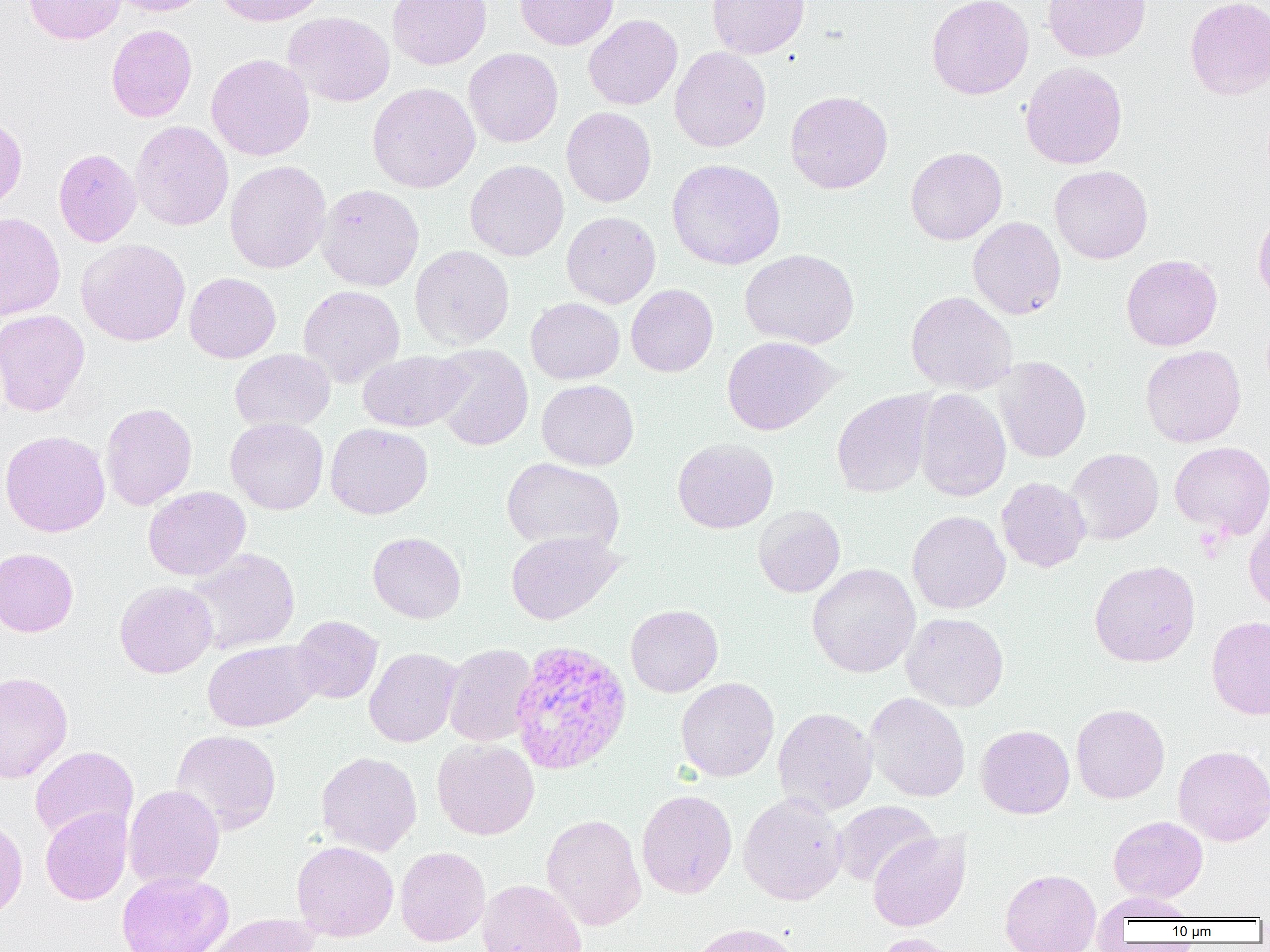
Approximate bounding boxes as (x1, y1, x2, y2) in pixels. Uninfected red blood cell locations: (24, 0, 125, 44), (110, 0, 210, 16), (214, 0, 331, 27), (387, 0, 491, 69), (515, 0, 619, 50), (706, 0, 809, 59), (926, 0, 1034, 99), (1042, 0, 1151, 62), (1184, 0, 1270, 100), (282, 11, 396, 107), (583, 14, 682, 109), (106, 24, 197, 122), (669, 46, 772, 152), (464, 48, 563, 148), (206, 53, 315, 161), (1020, 61, 1128, 169), (367, 82, 480, 193), (785, 90, 893, 194), (561, 107, 656, 207), (0, 111, 27, 212), (130, 120, 234, 231), (905, 147, 1007, 245), (53, 148, 142, 247), (465, 159, 569, 261), (667, 159, 786, 270), (224, 160, 331, 274), (1050, 165, 1153, 264), (316, 184, 424, 291), (1253, 210, 1270, 307), (561, 211, 661, 309), (0, 212, 65, 320), (968, 217, 1066, 320), (0, 220, 134, 323), (76, 239, 191, 346), (410, 245, 514, 350), (740, 249, 859, 349), (1121, 254, 1222, 351), (184, 272, 281, 363), (626, 284, 718, 377), (298, 285, 405, 387), (906, 291, 1017, 395), (525, 297, 624, 384), (0, 309, 90, 417), (721, 336, 839, 435), (431, 344, 534, 451), (1140, 345, 1246, 448), (229, 348, 335, 432), (357, 350, 471, 432), (993, 356, 1091, 463), (537, 379, 639, 471), (913, 388, 1011, 502), (831, 390, 936, 498), (100, 402, 197, 510), (226, 417, 328, 515), (325, 423, 433, 519), (1, 430, 110, 537), (672, 438, 778, 533), (1169, 441, 1270, 538), (1067, 448, 1164, 544), (501, 457, 625, 554), (997, 477, 1091, 572), (143, 486, 251, 580), (753, 504, 845, 598), (907, 510, 1011, 614), (1244, 512, 1270, 613), (505, 530, 624, 625), (367, 532, 467, 623), (185, 547, 301, 655), (0, 548, 78, 637), (1089, 559, 1201, 667), (807, 563, 920, 678), (115, 580, 218, 678), (625, 604, 723, 697), (901, 612, 1009, 712), (290, 615, 383, 704), (1206, 616, 1270, 719), (202, 639, 320, 732), (443, 643, 538, 746), (364, 647, 462, 747), (0, 671, 73, 783), (675, 677, 779, 782), (864, 692, 970, 802), (1071, 703, 1170, 804), (773, 707, 877, 816), (976, 724, 1075, 819), (170, 729, 282, 835), (432, 738, 539, 840), (1172, 745, 1270, 846), (29, 746, 139, 843), (316, 751, 422, 856), (123, 784, 224, 889), (636, 789, 737, 898), (738, 792, 848, 905), (833, 800, 939, 888), (40, 807, 132, 905), (0, 813, 27, 921), (541, 813, 646, 931), (1108, 816, 1208, 902), (868, 830, 971, 931), (291, 840, 399, 941), (395, 846, 490, 947), (1000, 868, 1101, 952), (116, 870, 234, 952), (477, 879, 588, 952), (1095, 892, 1198, 923), (200, 913, 319, 952), (686, 922, 805, 952), (872, 933, 962, 952). Plasmodium vivax-infected red blood cell locations: (511, 642, 634, 778). Slide-level diagnosis: Plasmodium vivax. Light microscopy. Single field of view. Thin blood film. Image is 1270×952 pixels. Captured at 1000x magnification.